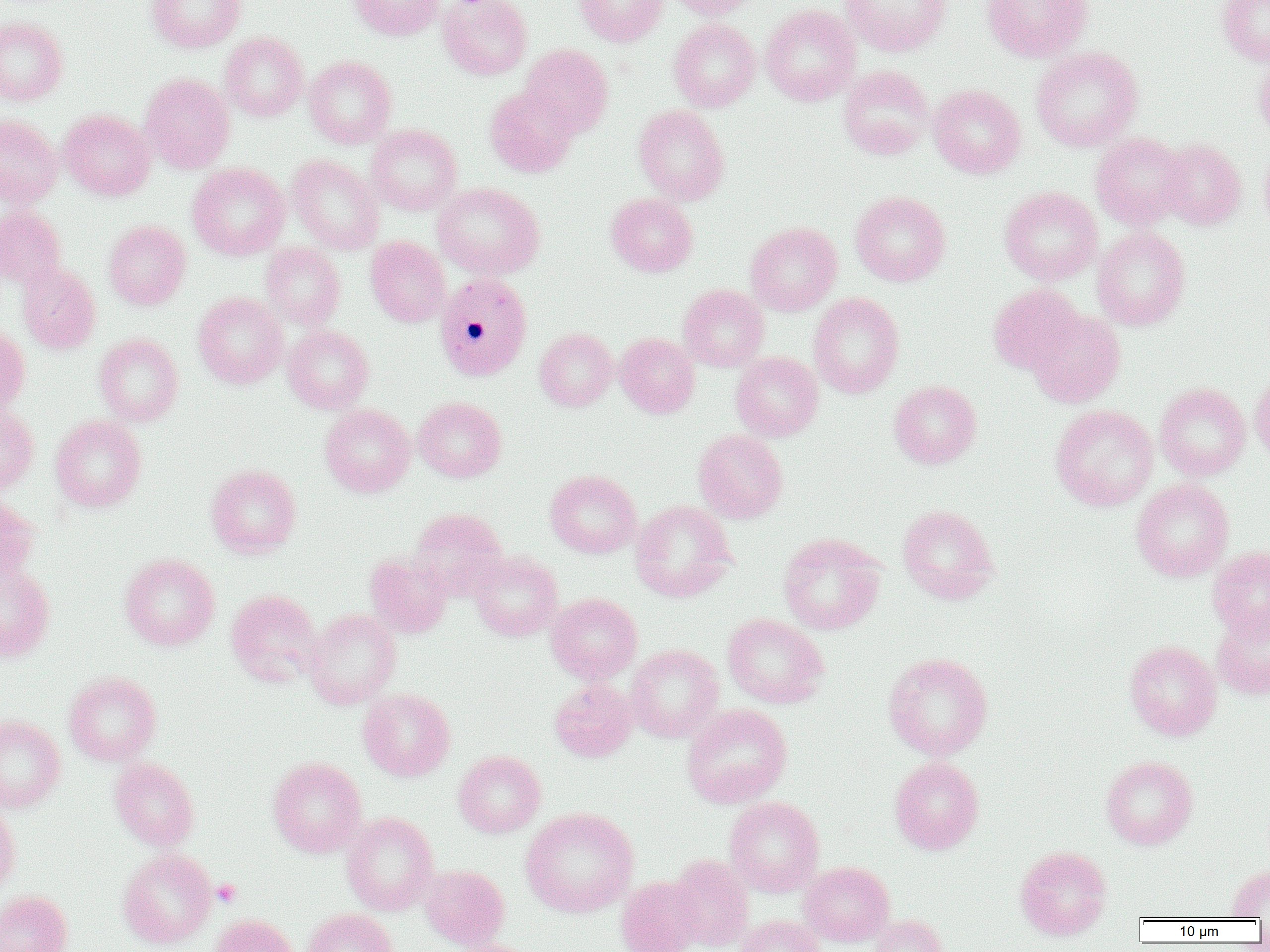
Approximate bounding boxes as [x1, y1, x2, y2] in pixels. Uninfected red blood cell locations: [147, 0, 245, 52], [349, 0, 443, 40], [438, 0, 532, 80], [574, 0, 669, 47], [667, 0, 763, 19], [840, 0, 952, 57], [981, 0, 1093, 62], [1217, 0, 1270, 65], [760, 4, 861, 106], [0, 16, 68, 105], [668, 19, 761, 112], [220, 31, 308, 121], [520, 44, 613, 138], [1031, 46, 1142, 151], [1254, 53, 1270, 148], [304, 56, 396, 148], [300, 57, 390, 252], [838, 65, 934, 160], [140, 72, 235, 173], [928, 84, 1026, 178], [485, 85, 578, 178], [633, 105, 729, 205], [59, 109, 155, 201], [0, 115, 62, 207], [366, 124, 462, 215], [1090, 132, 1190, 230], [1157, 139, 1247, 230], [1259, 144, 1270, 237], [287, 155, 383, 254], [187, 163, 290, 260], [433, 182, 544, 279], [999, 186, 1102, 286], [850, 190, 950, 287], [606, 193, 698, 277], [0, 204, 66, 288], [104, 220, 191, 310], [745, 222, 842, 316], [1092, 226, 1190, 331], [366, 236, 450, 327], [261, 243, 345, 329], [17, 262, 100, 354], [988, 283, 1085, 375], [678, 284, 769, 371], [193, 292, 288, 389], [808, 292, 904, 398], [1027, 310, 1125, 408], [0, 325, 29, 416], [282, 325, 374, 414], [535, 328, 617, 411], [94, 333, 183, 426], [615, 333, 699, 418], [731, 352, 823, 441], [1250, 370, 1270, 465], [889, 380, 982, 469], [1154, 383, 1250, 480], [413, 396, 506, 482], [320, 404, 416, 497], [1050, 404, 1158, 511], [0, 405, 38, 494], [50, 415, 146, 512], [693, 429, 787, 523], [206, 465, 301, 558], [545, 469, 642, 558], [1131, 479, 1234, 582], [0, 496, 40, 585], [630, 500, 737, 602], [897, 504, 1000, 605], [409, 508, 507, 600], [778, 533, 885, 635], [1208, 546, 1270, 641], [470, 551, 563, 641], [365, 552, 452, 638], [119, 553, 220, 650], [0, 564, 55, 661], [226, 589, 323, 688], [546, 592, 642, 683], [1212, 608, 1270, 701], [305, 609, 401, 709], [723, 613, 828, 708], [1124, 639, 1221, 740], [626, 644, 724, 742], [883, 652, 993, 760], [64, 671, 161, 766], [549, 680, 637, 762], [358, 689, 455, 781], [681, 703, 792, 808], [0, 715, 65, 812], [453, 751, 546, 837], [1101, 755, 1198, 849], [890, 756, 984, 854], [109, 757, 199, 850], [267, 757, 366, 857], [724, 796, 824, 896], [0, 802, 20, 900], [520, 807, 639, 917], [342, 812, 439, 915], [1015, 845, 1112, 940], [118, 848, 217, 948], [669, 855, 754, 951], [799, 862, 895, 947], [419, 864, 510, 950], [1227, 864, 1270, 919], [616, 876, 703, 952], [0, 890, 73, 952], [303, 908, 399, 952], [209, 914, 300, 952], [735, 914, 825, 952], [869, 914, 947, 952], [444, 939, 541, 952]. Platelet locations: [212, 880, 242, 907]. Plasmodium malariae-infected red blood cell locations: [434, 272, 532, 381]. Slide-level diagnosis: Plasmodium malariae. Captured at 1000x magnification. Single field of view. Thin blood film. Light microscopy. Image is 1270×952 pixels.